Assess this cell for malaria.
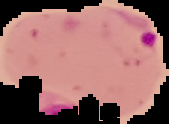

It is parasitized.

preparation = thin blood smear
image size = 169×124 pixels
image type = segmented cell region with the area outside set to black